State which parasite is depicted.
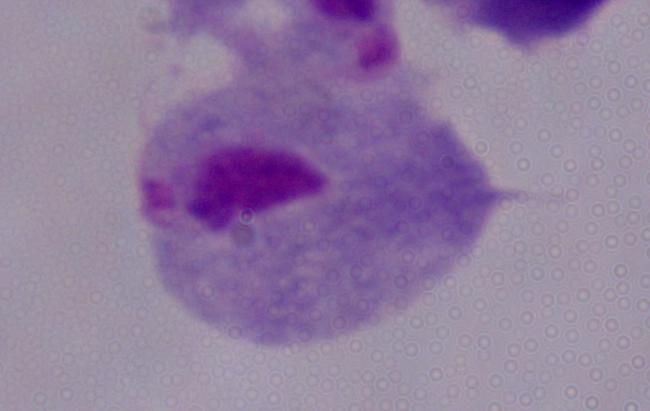
A trichomonad.

Captured at 1000x magnification. Micrograph.